Report the malaria status of this cell.
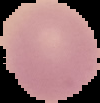

Uninfected.

image size = 100×103 pixels
preparation = thin blood smear
image type = segmented cell region with the area outside set to black